State which cell type is depicted.
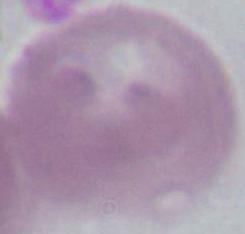

An erythrocyte.

modality = photomicrograph
magnification = 1000x